Report the malaria status of this cell.
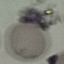

Uninfected.

stain = Giemsa
capture = smartphone through the microscope eyepiece
preparation = thin blood film
image type = cell patch, automatically extracted from a larger field of view and resized to 64 × 64 pixels